Identify the parasite.
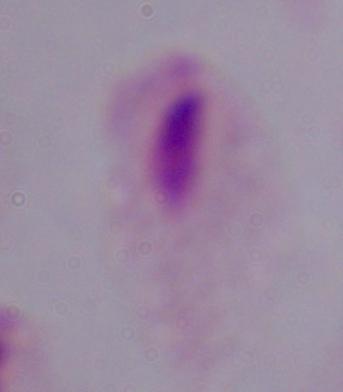
A trichomonad.

Photomicrograph. Captured at 1000x magnification.